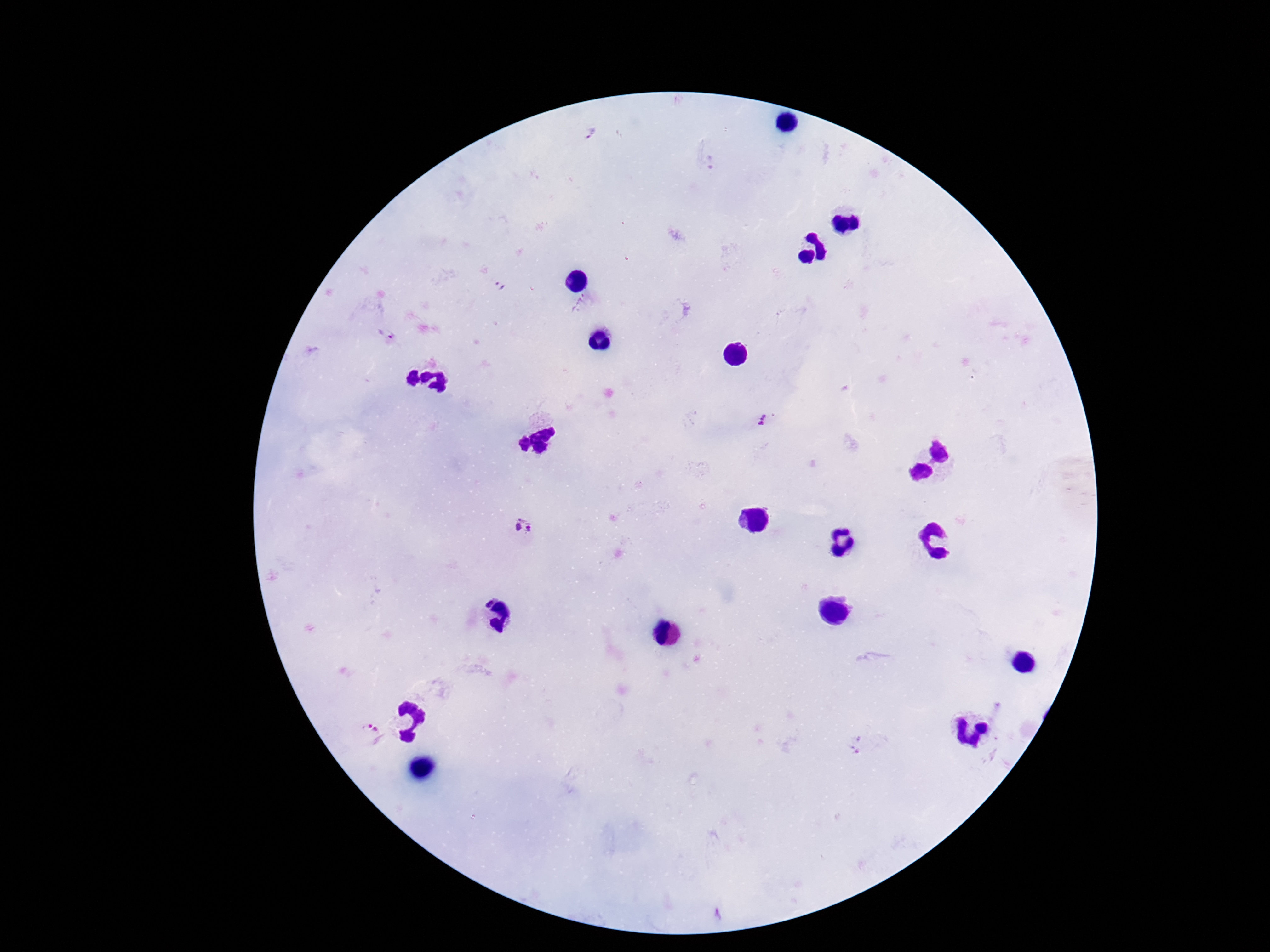
preparation = thick peripheral-blood smear
Plasmodium parasite locations = approximate centers as (x, y) in pixels: (588, 131), (711, 163), (502, 287), (387, 334), (763, 420), (525, 529), (369, 734), (858, 745)
field of view = single
magnification = 100x
image size = 1270×952 pixels
capture = smartphone camera through the microscope eyepiece
patient malaria status = infected
stain = Giemsa